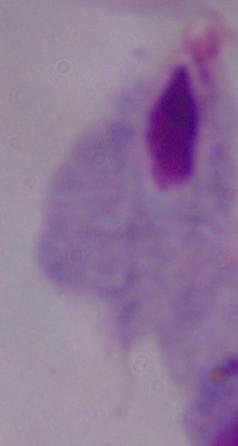

{
  "identification": "trichomonad",
  "modality": "photomicrograph",
  "magnification": "1000x"
}